Identify the parasite.
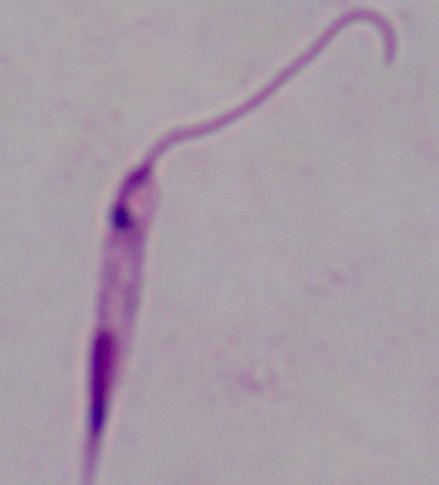
This is Leishmania.

1000x magnification. Micrograph.